Give the position of every malaria parasite.
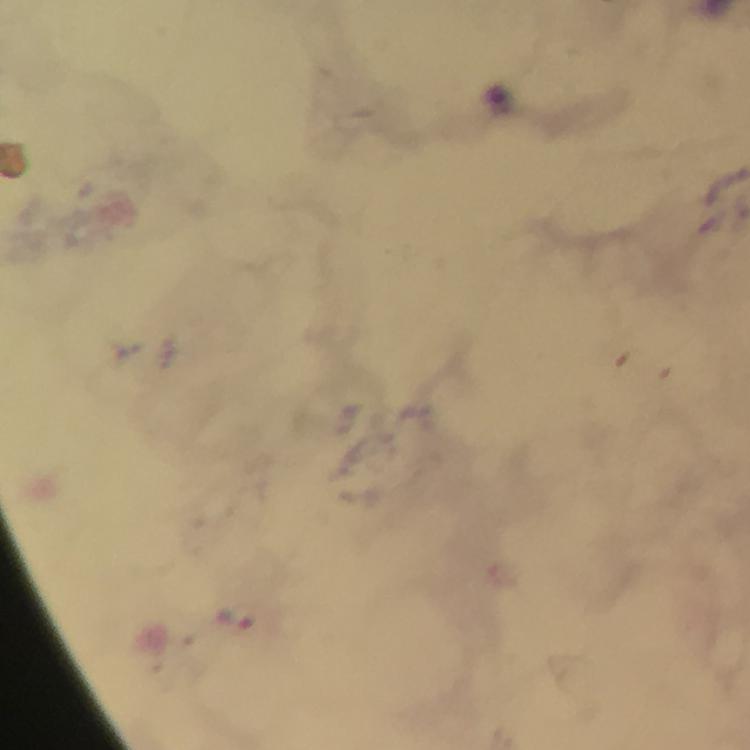
Approximate centers as {x, y} in pixels.
Malaria parasites: {234, 616}.

image size = 750×750 pixels
magnification = 100x
context = from a diagnostic examination for malaria
immersion oil = applied
stain = Giemsa
preparation = thick smear
capture = smartphone mounted on the microscope
cropped from = one field of view